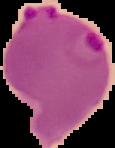 From a thin blood film. Image is 115×148 pixels. Segmented cell region on a black background. Result: malaria parasites identified.